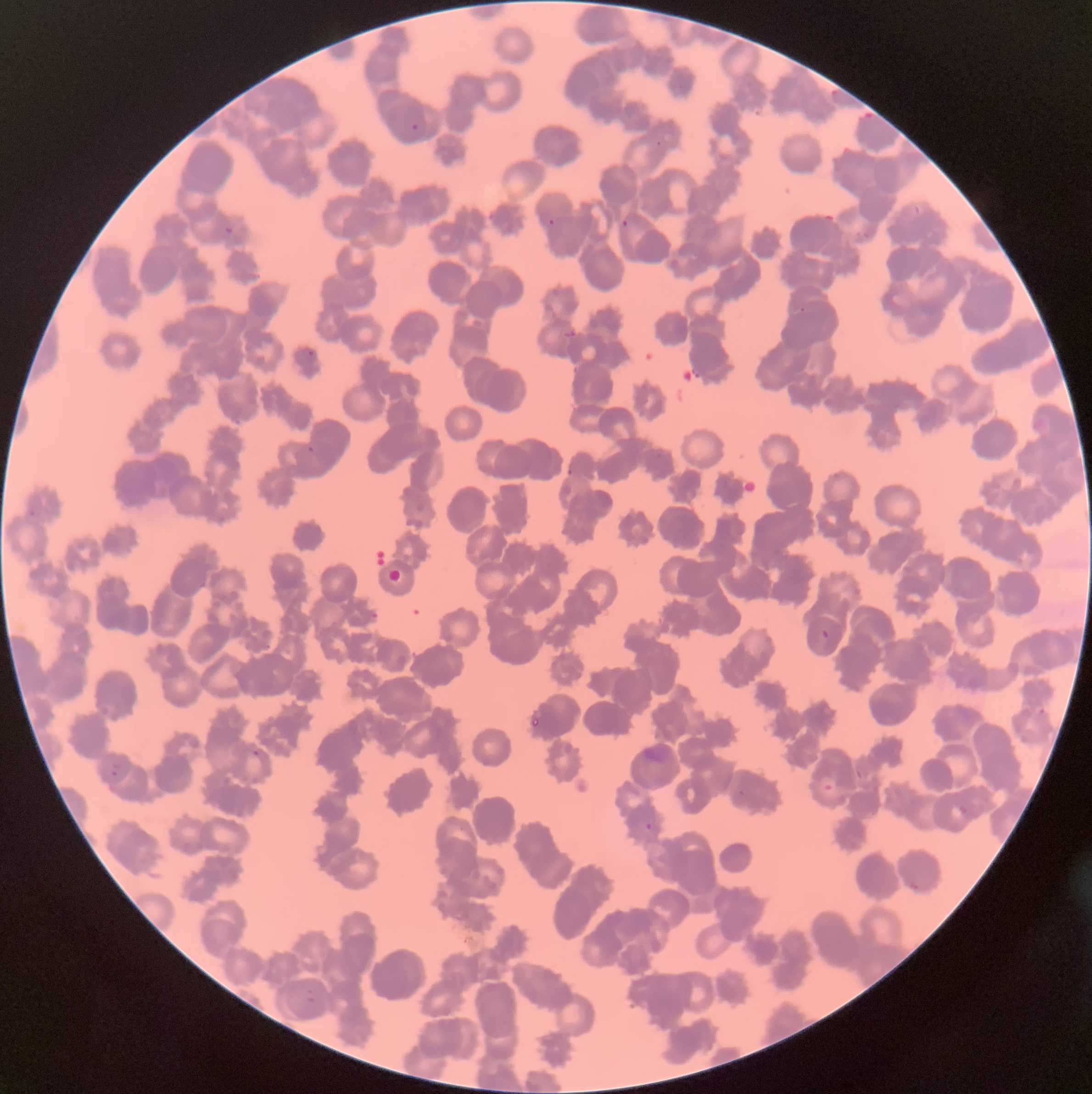
Summary:
  - Coordinate format: approximate bounding boxes as (x1,y1)-(x2,y2) corner pairs in pixels
  - Plasmodium parasites too small for a box (approximate centers as (x,y) in pixels): (659,143), (551,222), (802,310), (570,472)
  - Plasmodium parasite locations: (829,85)-(842,100), (859,110)-(876,122), (410,123)-(419,130), (621,219)-(629,227), (224,225)-(236,236), (306,349)-(317,358), (307,446)-(315,453), (28,510)-(37,518), (821,629)-(830,640), (1036,707)-(1048,718), (251,750)-(259,758), (110,762)-(119,777), (855,769)-(864,780), (738,790)-(746,797), (956,802)-(969,817), (645,822)-(653,831), (905,879)-(921,892), (303,989)-(316,1004)
  - Red blood cell morphology: rouleaux formation
  - Preparation: thin blood film
  - Image size: 1092×1094 pixels
  - Modality: light microscopy